Give a bounding box for every malaria parasite.
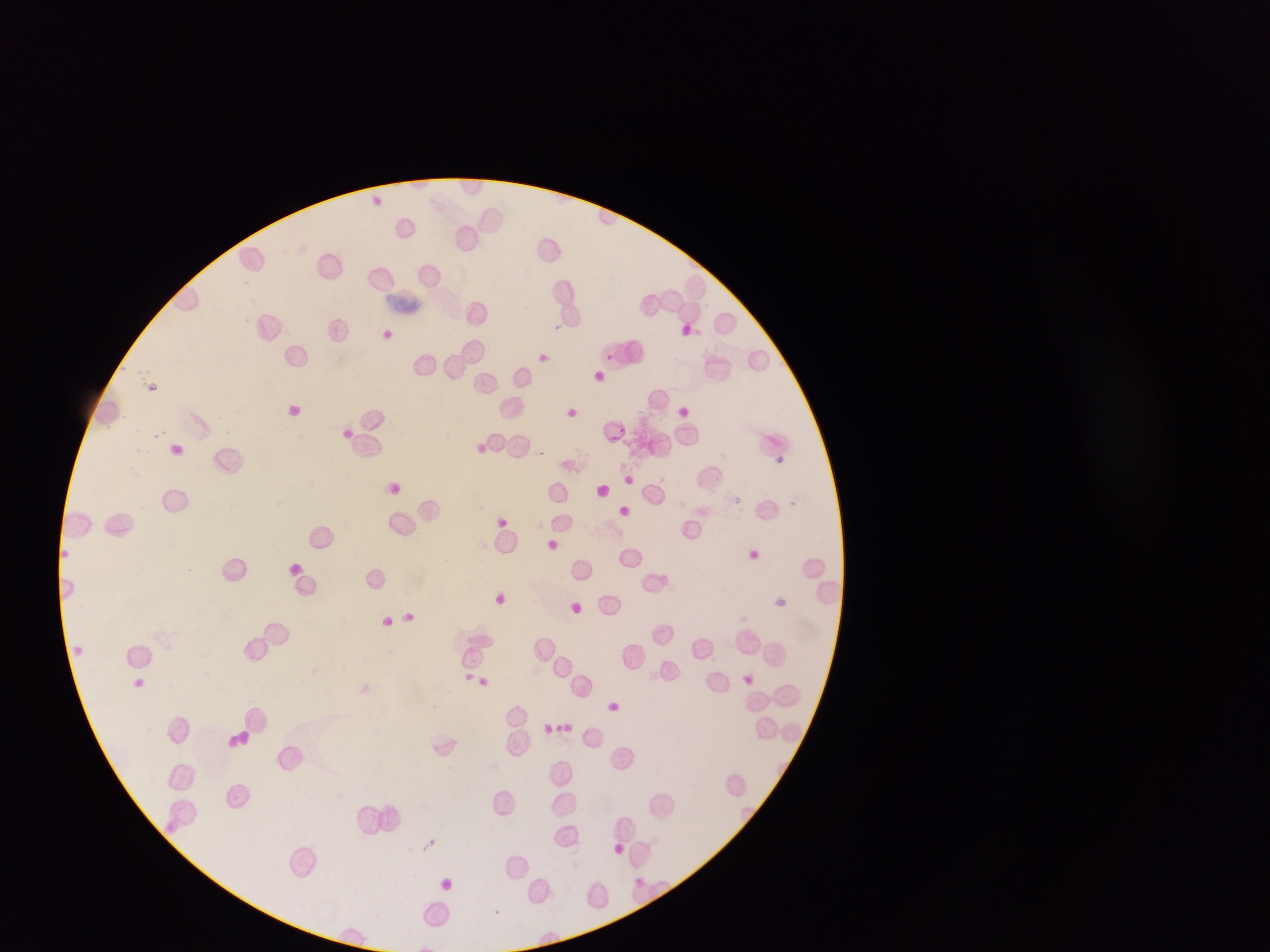
Approximate bounding boxes as {left, top, right, bottom} in pixels.
Malaria parasites: {552, 322, 571, 333}, {602, 351, 615, 364}, {618, 425, 629, 433}, {608, 434, 628, 448}, {788, 498, 801, 514}, {633, 877, 644, 888}.

capture: mobile-phone photograph through a microscope
field_of_view: single
country: Ghana
preparation: thin blood film
image_size: 1270×952 pixels